Locate every Plasmodium parasite.
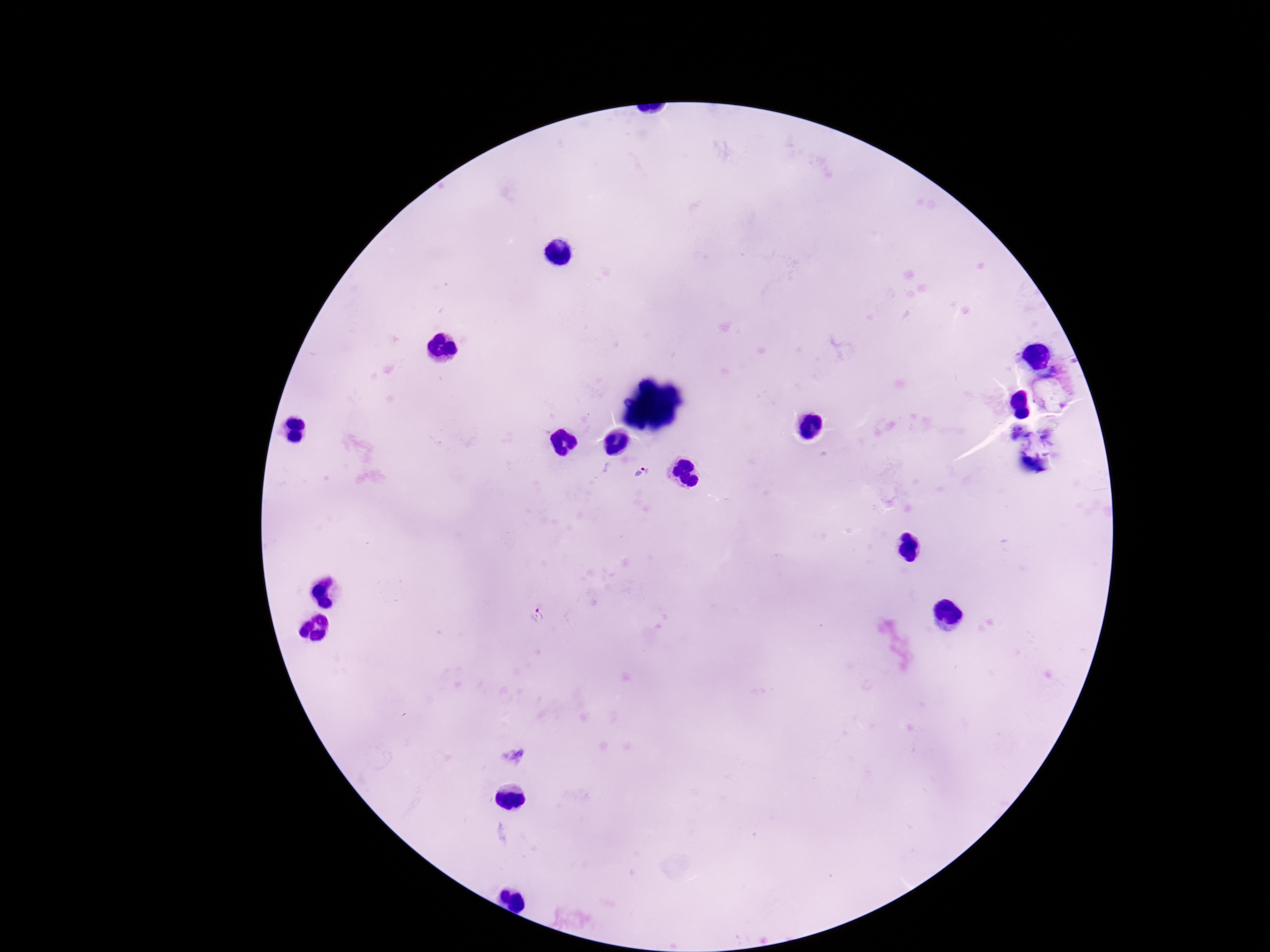
Approximate centers as [x, y] in pixels.
Plasmodium parasites: [641, 473], [534, 615].

Smartphone photograph taken through the microscope eyepiece. Giemsa-stained preparation. Image is 1270×952 pixels. One field from this slide. 100x magnification. Thick blood film. Patient malaria status: positive.